Name the parasite shown.
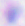
Toxoplasma gondii.

Summary:
  - Magnification: 400x
  - Modality: micrograph